Classify this cell by malaria status.
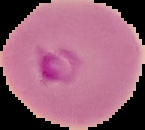
Parasitized.

preparation = thin blood film
image type = segmented cell region on a black background
image size = 145×130 pixels